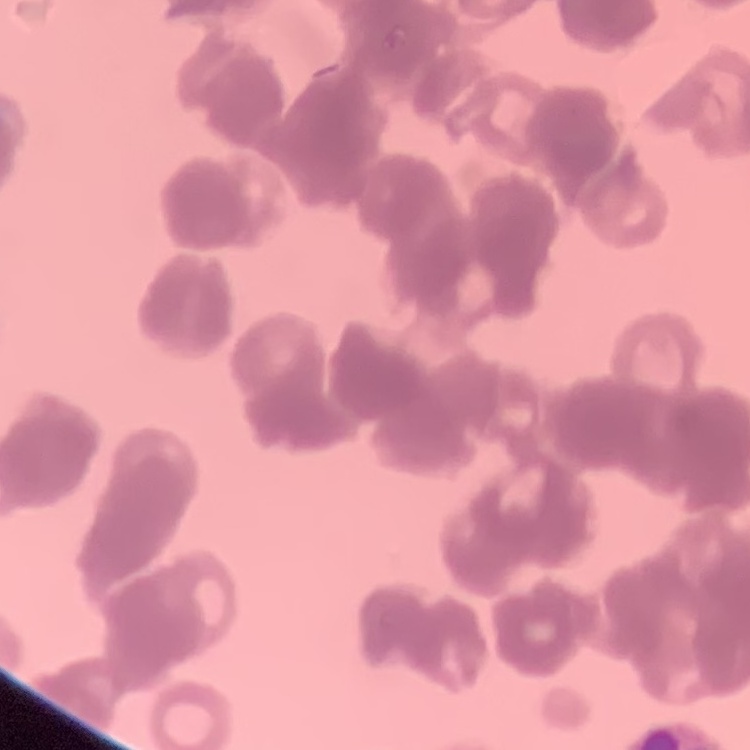
Summary:
  - Erythrocyte morphology: rouleaux formation
  - Preparation: thin blood smear
  - Image type: one tile cut from a larger photomicrograph
  - Stain: Field's or Giemsa